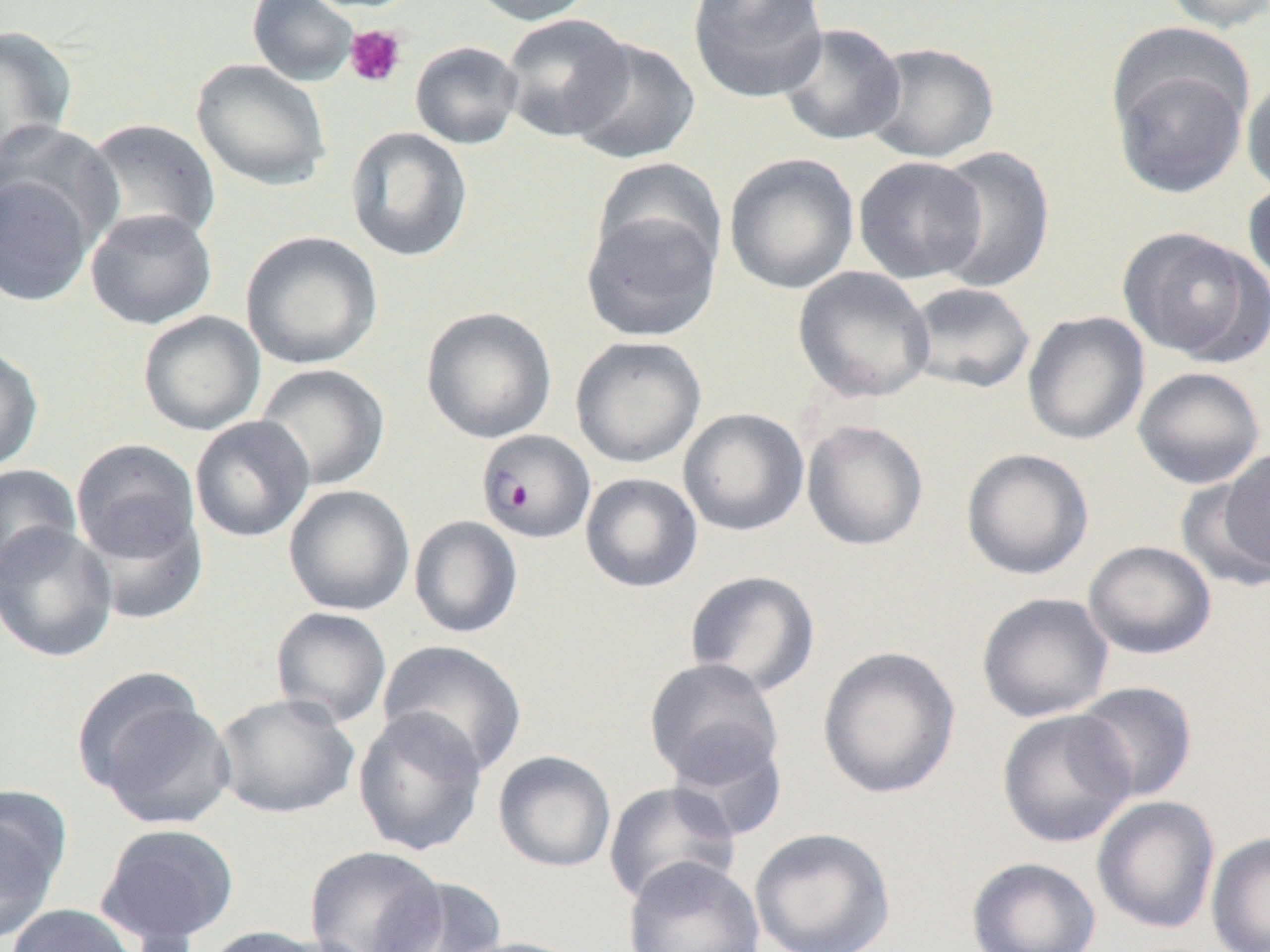
Approximate bounding boxes as (x1, y1, x2, y2) in pixels. Plasmodium falciparum-infected red blood cell locations: (475, 429, 597, 544). Platelet locations: (344, 25, 407, 88). Uninfected red blood cell locations: (247, 0, 360, 87), (465, 0, 597, 26), (687, 0, 829, 103), (1161, 0, 1270, 33), (500, 13, 634, 142), (777, 22, 907, 146), (0, 25, 78, 168), (566, 37, 701, 165), (410, 41, 524, 149), (863, 41, 999, 164), (1109, 51, 1251, 199), (191, 58, 332, 191), (1241, 74, 1270, 198), (1, 118, 119, 252), (83, 118, 221, 247), (345, 126, 473, 262), (929, 145, 1056, 294), (723, 153, 860, 295), (853, 155, 988, 284), (590, 156, 728, 276), (0, 173, 96, 307), (1242, 178, 1270, 292), (85, 208, 218, 330), (581, 208, 720, 342), (1118, 227, 1267, 364), (240, 231, 383, 370), (792, 266, 935, 404), (903, 281, 1035, 395), (420, 306, 557, 444), (1022, 310, 1150, 446), (137, 311, 266, 436), (570, 335, 707, 468), (0, 345, 45, 474), (254, 363, 390, 491), (1132, 366, 1266, 489), (678, 407, 809, 537), (189, 415, 316, 543), (801, 419, 929, 551), (70, 438, 201, 564), (1217, 447, 1270, 579), (961, 448, 1094, 580), (0, 463, 82, 582), (579, 472, 703, 593), (1177, 473, 1269, 593), (283, 484, 415, 616), (79, 505, 208, 625), (408, 515, 523, 639), (0, 522, 118, 662), (1082, 540, 1217, 659), (684, 569, 820, 697), (976, 592, 1114, 722), (270, 607, 392, 729), (377, 639, 528, 776), (817, 645, 961, 799), (644, 657, 784, 791), (79, 679, 237, 830), (1071, 681, 1197, 803), (213, 692, 360, 820), (352, 707, 488, 857), (996, 709, 1136, 848), (665, 733, 789, 841), (492, 750, 617, 872), (603, 781, 740, 906), (0, 787, 71, 940), (1091, 795, 1220, 934), (95, 822, 240, 947), (748, 826, 896, 952), (1206, 832, 1270, 952), (303, 845, 447, 952), (966, 856, 1101, 952), (624, 857, 764, 952), (374, 878, 508, 952), (6, 903, 143, 952), (199, 925, 337, 951), (446, 936, 591, 952). Slide-level diagnosis: Plasmodium falciparum. Image is 1270×952 pixels. Optical microscopy. Captured at 1000x magnification. Thin blood smear. Single field of view.